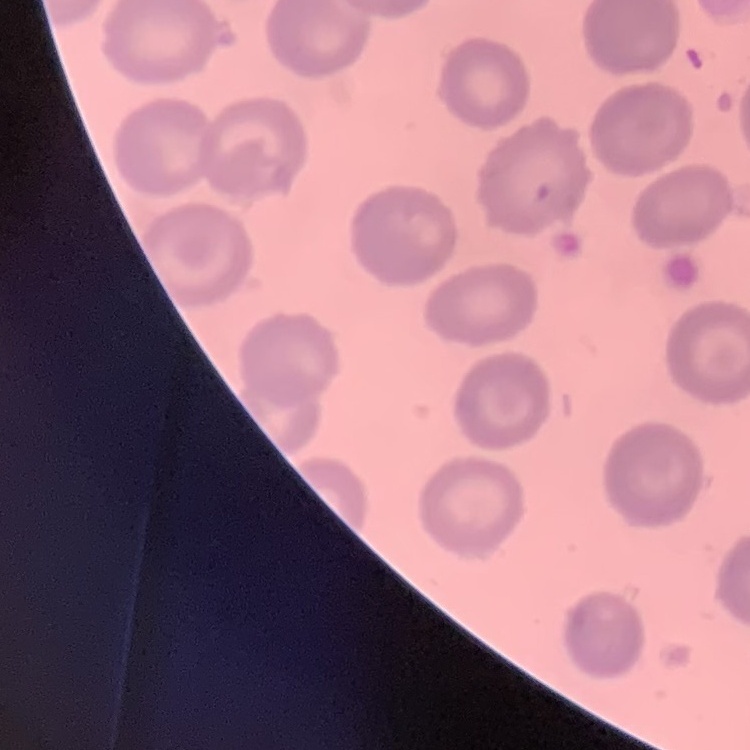

{
  "erythrocyte_morphology": "no rouleaux formation",
  "preparation": "thin blood film",
  "image_type": "one tile cut from a larger photomicrograph",
  "stain": "Field's or Giemsa"
}